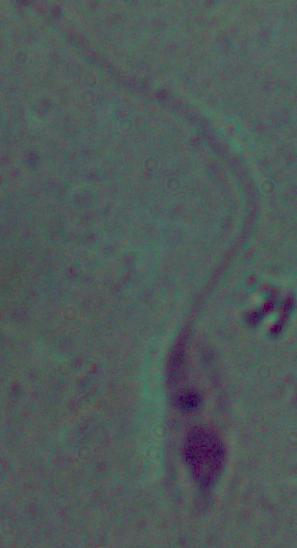
Summary:
  - Magnification: 1000x
  - Modality: micrograph
  - Identification: Leishmania